Name the cell type shown.
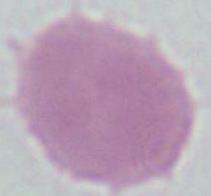

This is an erythrocyte.

Summary:
  - Modality: micrograph
  - Magnification: 1000x